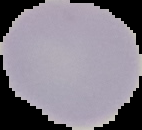
Summary:
  - Preparation: thin blood smear
  - Image size: 142×130 pixels
  - Result: negative for malaria parasites
  - Image type: segmented cell region on a black background